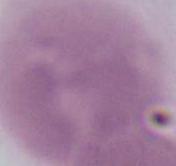 An erythrocyte is seen. Photomicrograph. Captured at 1000x magnification.